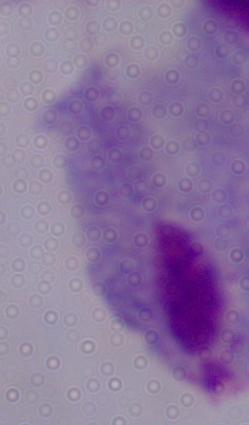

Summary:
  - Identification: trichomonad
  - Magnification: 1000x
  - Modality: photomicrograph